Comment on the morphology of the erythrocytes.
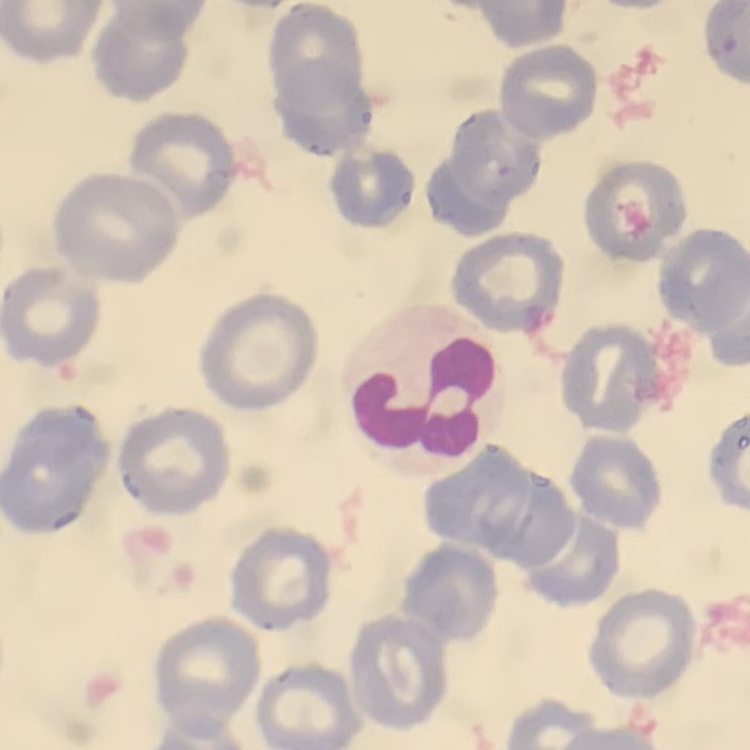

No rouleaux formation.

Field's or Giemsa stain. One tile cut from a larger photomicrograph. Thin blood film.